Identify the preparation type.
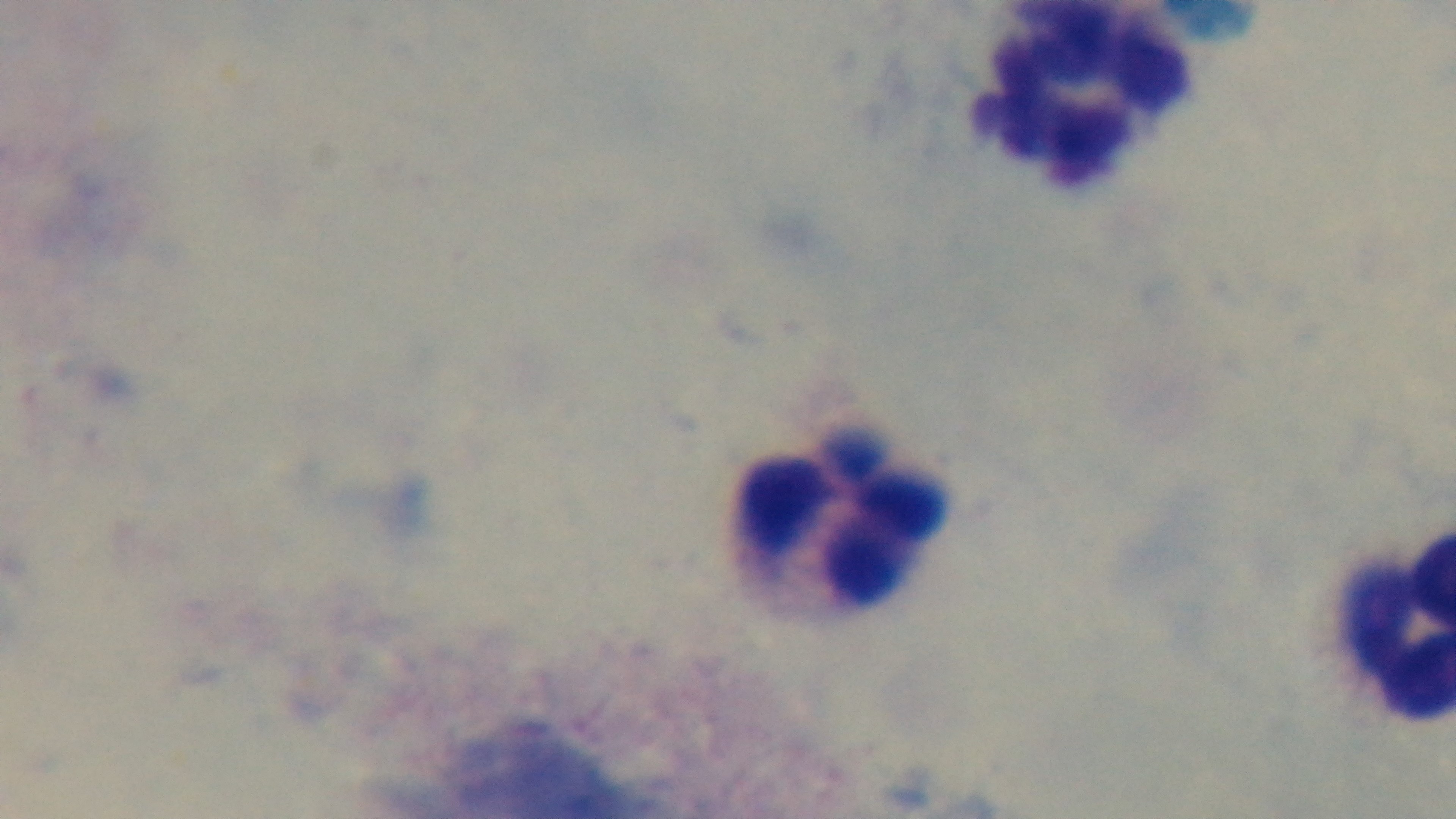

A thick smear.

Oil-immersion objective, 100x. Captured with a mounted 4K digital camera. Malaria status: negative. Giemsa-stained. Light microscopy. Single field of view.